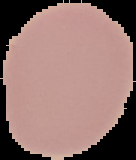 Image is 136×160 pixels. Malaria status: uninfected. The area outside the segmented cell region is set to black. From a thin blood film.